Describe the morphology of the erythrocytes.
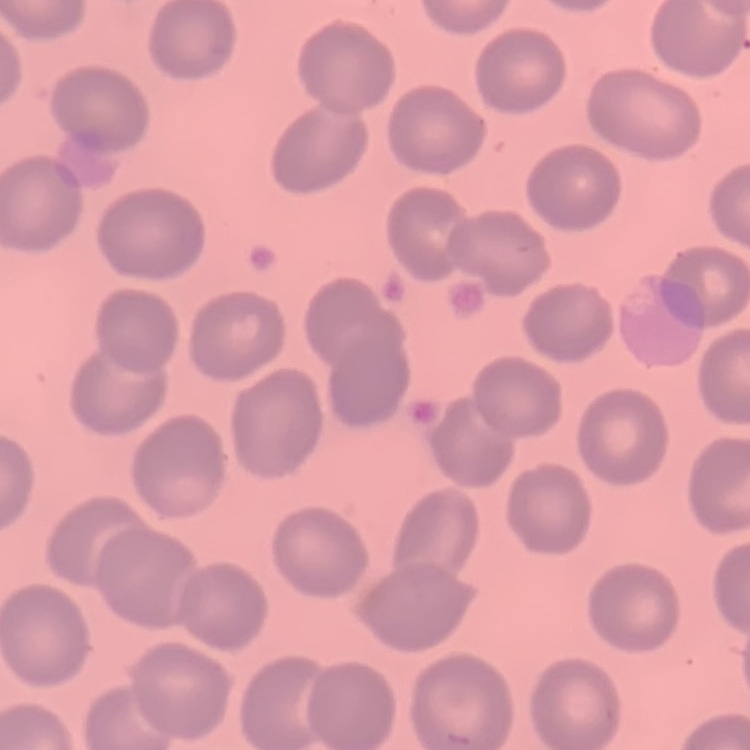
They show no rouleaux formation.

Field's or Giemsa stain. Thin blood film. Square crop of a larger photomicrograph.